Name the blood parasite species.
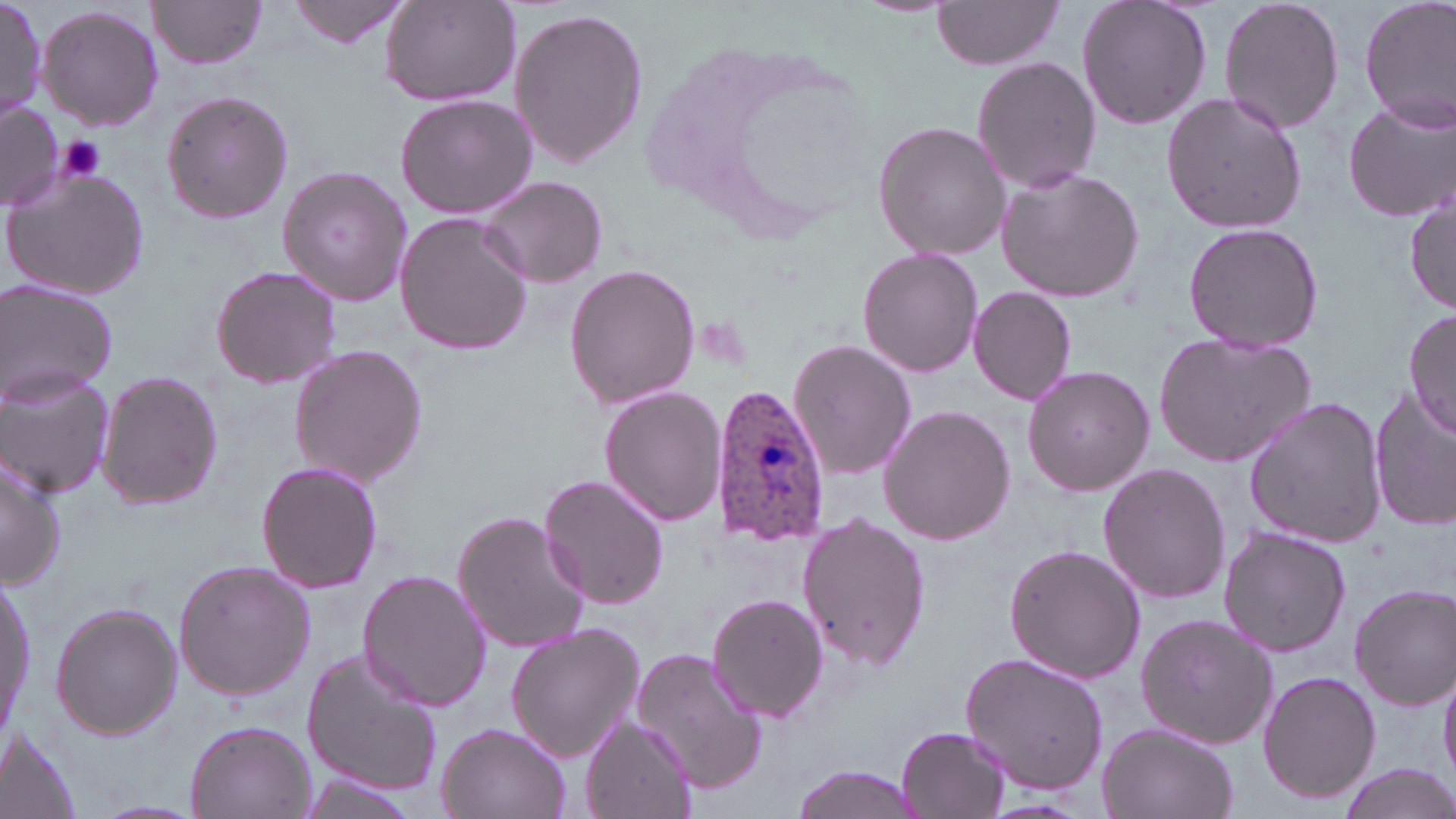
Plasmodium ovale.

Approximate bounding boxes as (x1, y1, x2, y2) in pixels. Platelet locations: (55, 137, 108, 184). Plasmodium ovale-infected red blood cell locations: (710, 385, 830, 547). Uninfected red blood cell locations: (149, 0, 269, 70), (288, 0, 412, 49), (379, 0, 520, 106), (1075, 0, 1212, 131), (1217, 0, 1346, 136), (1359, 0, 1456, 132), (0, 1, 47, 121), (930, 1, 1066, 70), (37, 4, 164, 132), (508, 6, 649, 170), (972, 56, 1100, 194), (1160, 89, 1308, 235), (160, 90, 294, 225), (393, 94, 537, 219), (1343, 97, 1455, 224), (0, 103, 60, 210), (873, 121, 1010, 261), (275, 164, 412, 308), (3, 165, 153, 302), (995, 167, 1145, 303), (479, 176, 609, 289), (1405, 183, 1455, 314), (396, 213, 530, 356), (1181, 221, 1323, 355), (857, 247, 985, 378), (563, 262, 701, 410), (209, 264, 344, 390), (0, 279, 118, 406), (968, 286, 1077, 405), (1404, 307, 1456, 444), (1152, 331, 1317, 469), (788, 339, 917, 481), (287, 344, 427, 487), (1021, 364, 1155, 498), (0, 367, 114, 498), (96, 369, 224, 510), (600, 387, 729, 525), (1368, 388, 1455, 531), (1243, 396, 1389, 548), (877, 404, 1016, 546), (0, 447, 67, 589), (256, 460, 383, 595), (1099, 462, 1230, 605), (538, 471, 670, 610), (453, 509, 591, 656), (798, 511, 931, 672), (1218, 526, 1352, 657), (1003, 542, 1145, 685), (173, 560, 316, 699), (2, 564, 35, 746), (357, 570, 490, 712), (1349, 583, 1455, 710), (707, 593, 829, 723), (50, 603, 183, 741), (1135, 614, 1280, 749), (505, 622, 645, 763), (630, 647, 772, 794), (302, 649, 444, 798), (958, 652, 1108, 797), (1439, 662, 1456, 785), (1256, 669, 1381, 805), (580, 716, 695, 819), (186, 719, 315, 819), (1096, 722, 1239, 819), (437, 723, 569, 819), (896, 724, 1012, 819), (0, 732, 84, 819), (1335, 764, 1456, 819), (787, 765, 927, 819), (298, 776, 412, 817). May-Grünwald-Giemsa-stained preparation. Image is 1456×819 pixels. One field of a larger specimen. Light microscopy. Thin blood smear. Captured at 1000x magnification.